Give the extent of all Plasmodium malariae-infected red blood cells.
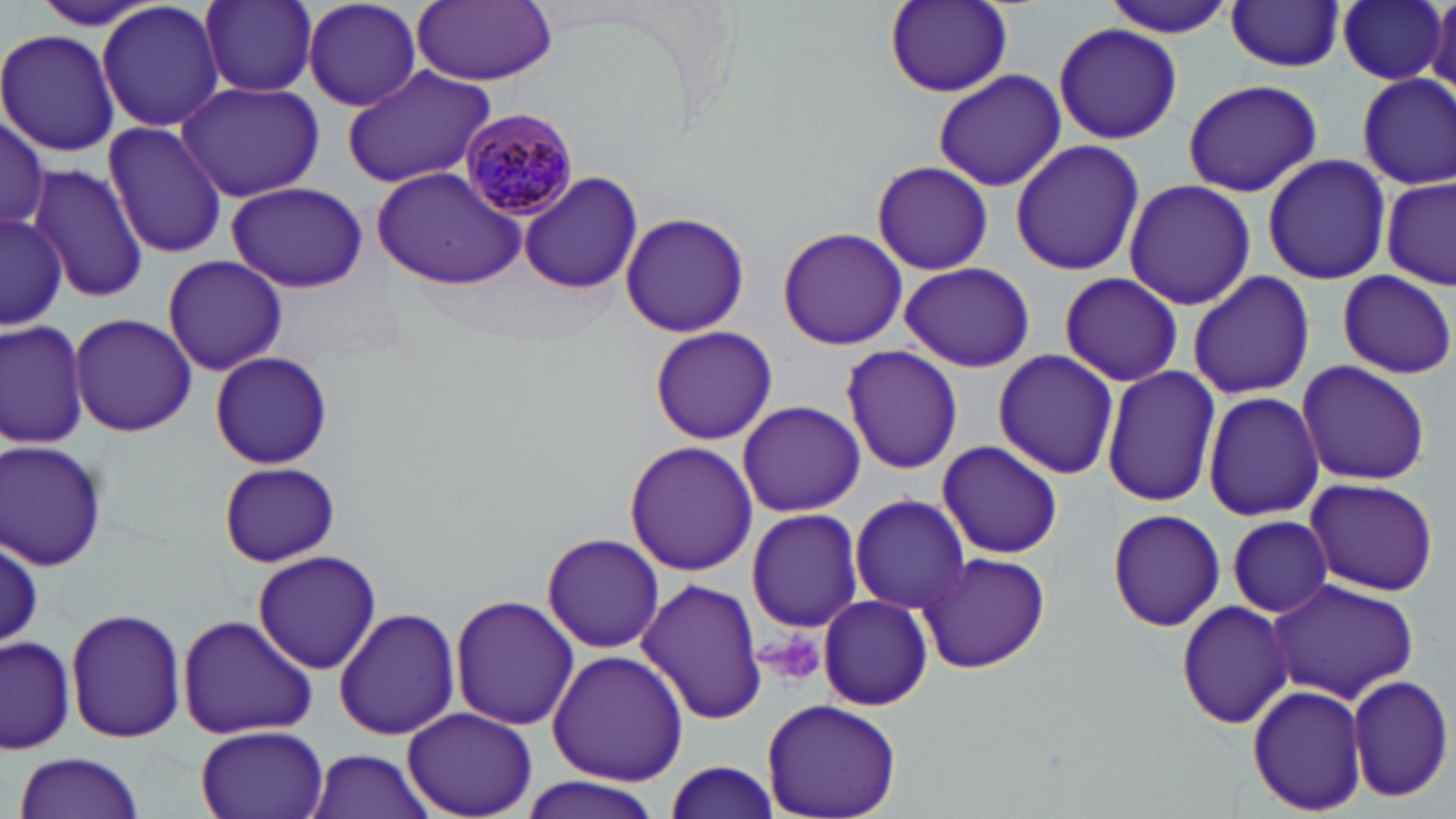
Approximate bounding boxes as named x1/y1/x2/y2 corners in pixels.
Plasmodium malariae-infected red blood cells: (x1=459, y1=108, x2=579, y2=219).

{
  "slide_level_diagnosis": "Plasmodium malariae",
  "image_size": "1456×819 pixels",
  "uninfected_red_blood_cell_locations": "approximate bounding boxes as named x1/y1/x2/y2 corners in pixels: (x1=1102, y1=0, x2=1241, y2=37), (x1=1337, y1=0, x2=1446, y2=85), (x1=1429, y1=0, x2=1456, y2=93), (x1=97, y1=1, x2=225, y2=134), (x1=196, y1=1, x2=321, y2=98), (x1=302, y1=1, x2=425, y2=113), (x1=410, y1=1, x2=559, y2=85), (x1=885, y1=1, x2=1014, y2=98), (x1=1225, y1=1, x2=1345, y2=71), (x1=1055, y1=23, x2=1181, y2=142), (x1=0, y1=29, x2=121, y2=157), (x1=340, y1=64, x2=498, y2=190), (x1=932, y1=69, x2=1065, y2=192), (x1=1355, y1=71, x2=1455, y2=191), (x1=1182, y1=78, x2=1323, y2=198), (x1=175, y1=81, x2=325, y2=204), (x1=0, y1=111, x2=49, y2=239), (x1=102, y1=122, x2=228, y2=260), (x1=1010, y1=139, x2=1144, y2=276), (x1=1262, y1=153, x2=1391, y2=285), (x1=871, y1=160, x2=992, y2=275), (x1=27, y1=164, x2=149, y2=303), (x1=372, y1=167, x2=527, y2=289), (x1=518, y1=171, x2=644, y2=295), (x1=1123, y1=177, x2=1254, y2=312), (x1=1381, y1=178, x2=1454, y2=288), (x1=226, y1=182, x2=370, y2=294), (x1=2, y1=208, x2=66, y2=332), (x1=618, y1=211, x2=751, y2=337), (x1=778, y1=227, x2=909, y2=350), (x1=160, y1=254, x2=289, y2=376), (x1=898, y1=260, x2=1035, y2=373), (x1=1336, y1=270, x2=1454, y2=379), (x1=1058, y1=271, x2=1181, y2=386), (x1=1187, y1=271, x2=1315, y2=399), (x1=70, y1=313, x2=196, y2=436), (x1=1, y1=318, x2=89, y2=449), (x1=648, y1=326, x2=779, y2=444), (x1=839, y1=346, x2=961, y2=476), (x1=991, y1=349, x2=1117, y2=480), (x1=210, y1=352, x2=332, y2=469), (x1=1296, y1=359, x2=1431, y2=487), (x1=1101, y1=365, x2=1220, y2=508), (x1=1202, y1=390, x2=1324, y2=522), (x1=737, y1=399, x2=865, y2=516), (x1=0, y1=440, x2=108, y2=572), (x1=937, y1=440, x2=1063, y2=560), (x1=624, y1=441, x2=758, y2=577), (x1=219, y1=461, x2=339, y2=566), (x1=1303, y1=476, x2=1439, y2=597), (x1=849, y1=496, x2=972, y2=615), (x1=1106, y1=506, x2=1226, y2=632), (x1=746, y1=507, x2=865, y2=633), (x1=1226, y1=515, x2=1333, y2=617), (x1=542, y1=533, x2=664, y2=653), (x1=2, y1=538, x2=44, y2=646), (x1=252, y1=550, x2=381, y2=675), (x1=916, y1=551, x2=1051, y2=675), (x1=1264, y1=576, x2=1420, y2=704), (x1=637, y1=578, x2=769, y2=727), (x1=818, y1=594, x2=933, y2=712), (x1=450, y1=595, x2=580, y2=730), (x1=1174, y1=601, x2=1293, y2=727), (x1=65, y1=606, x2=187, y2=744), (x1=334, y1=607, x2=462, y2=741), (x1=176, y1=612, x2=317, y2=742), (x1=0, y1=632, x2=77, y2=755), (x1=547, y1=649, x2=689, y2=786), (x1=1348, y1=674, x2=1453, y2=802), (x1=1248, y1=680, x2=1367, y2=817), (x1=762, y1=700, x2=902, y2=819), (x1=403, y1=707, x2=537, y2=818), (x1=194, y1=724, x2=329, y2=819), (x1=303, y1=749, x2=436, y2=819), (x1=13, y1=752, x2=146, y2=819), (x1=661, y1=757, x2=782, y2=818), (x1=517, y1=776, x2=665, y2=819)",
  "field_of_view": "single",
  "platelet_locations": "approximate bounding boxes as named x1/y1/x2/y2 corners in pixels: (x1=759, y1=628, x2=827, y2=688)",
  "preparation": "thin blood film",
  "modality": "optical microscopy",
  "magnification": "1000x",
  "stain": "May-Grünwald-Giemsa"
}